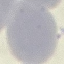
result = negative for malaria parasites
stain = Giemsa
preparation = thin smear
image type = cell patch, automatically extracted from a larger field of view and resized to 64 × 64 pixels
capture = smartphone through the microscope eyepiece